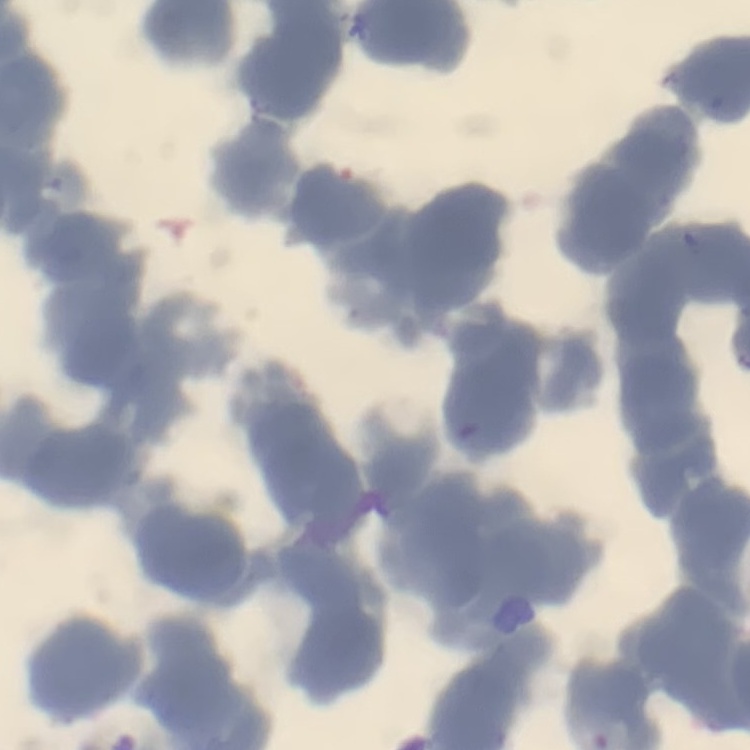

Summary:
  - Red blood cell morphology: rouleaux formation
  - Preparation: thin blood film
  - Image type: square crop of a larger photomicrograph
  - Stain: Field's or Giemsa